Assess this cell for malaria.
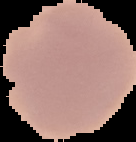
It is uninfected.

image_size: 136×142 pixels
image_type: cell region segmented out of the field of view; surrounding area masked to black
preparation: thin blood smear